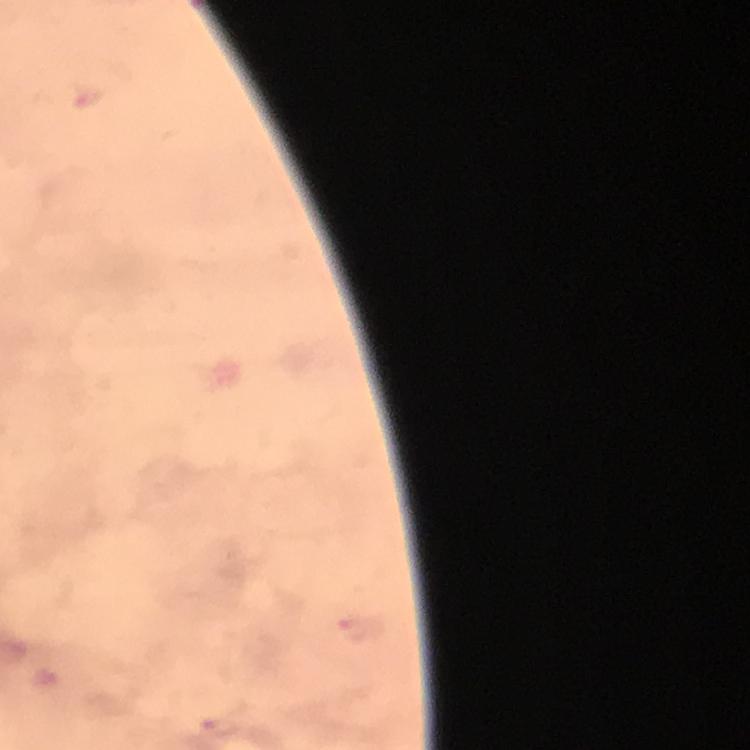

{
  "image_size": "750×750 pixels",
  "preparation": "thick blood film",
  "stain": "Giemsa",
  "plasmodium_parasite_locations": "approximate centers as (x, y) in pixels: (356, 631)",
  "cropped_from": "one field of view",
  "context": "from a diagnostic examination for malaria",
  "capture": "smartphone mounted on the microscope",
  "magnification": "100x",
  "immersion_oil": "used"
}